Comment on the morphology of the erythrocytes.
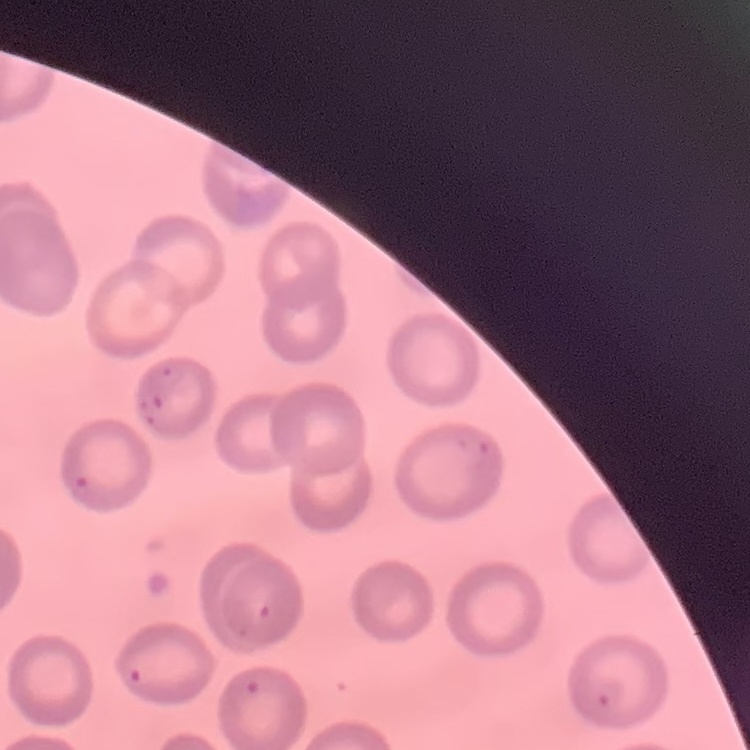
No rouleaux formation.

Thin peripheral smear. Square crop of a larger photomicrograph. Field's or Giemsa stain.